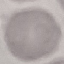
malaria status = uninfected
capture = smartphone through the microscope eyepiece
preparation = thin smear
image type = cell patch, automatically extracted from a larger field of view and resized to 64 × 64 pixels
stain = Giemsa